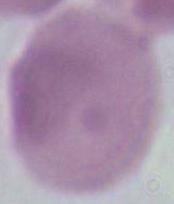
identification = erythrocyte
magnification = 1000x
modality = photomicrograph